Locate every Plasmodium parasite.
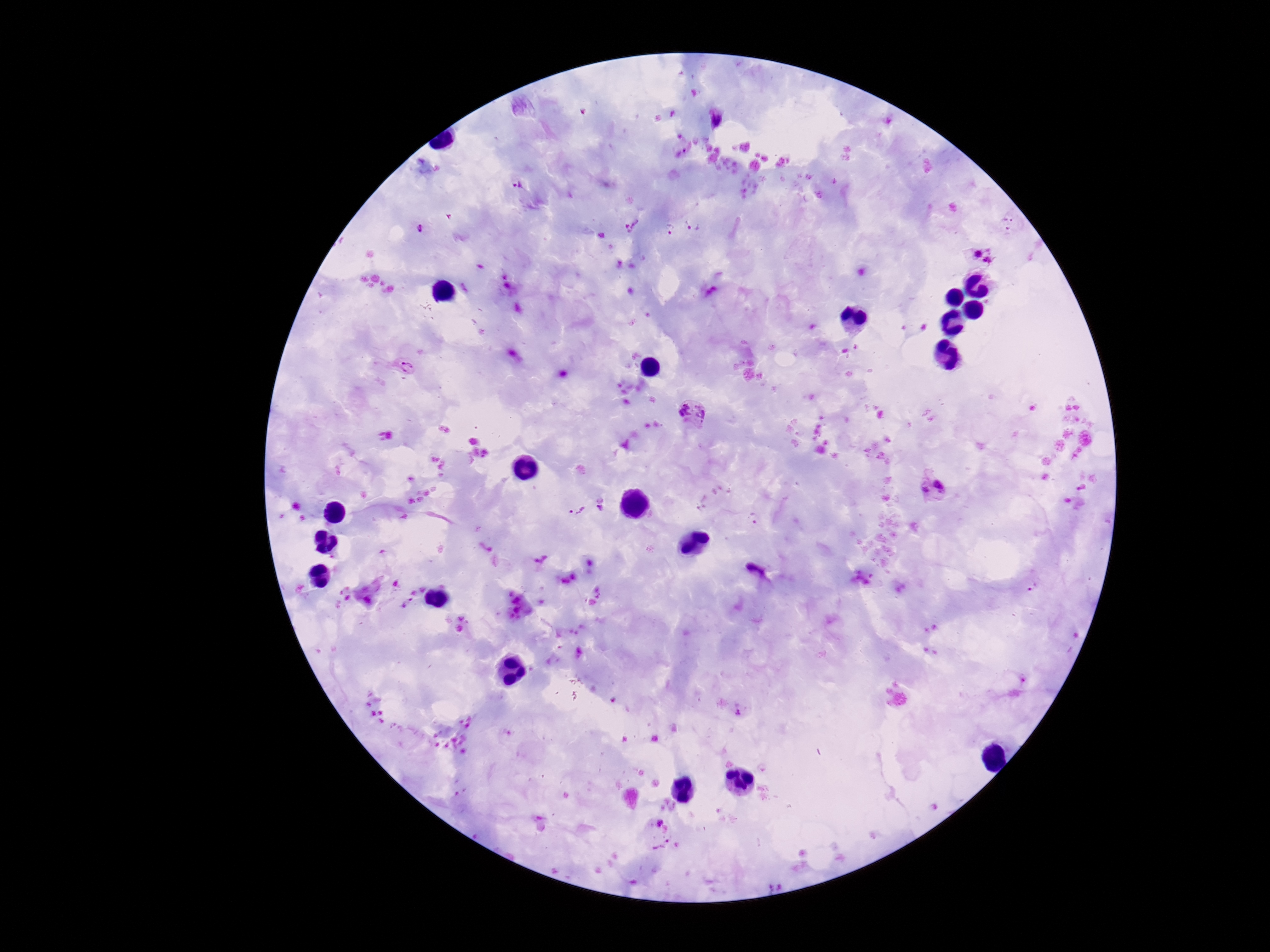

Approximate centers as [x, y] in pixels.
Plasmodium parasites: [718, 118], [517, 185], [1010, 221], [629, 224], [694, 224], [668, 227], [421, 228], [980, 256], [407, 368], [695, 415], [935, 489], [603, 505], [573, 509], [1031, 584], [406, 603], [738, 707], [658, 834].

capture = smartphone camera through the microscope eyepiece
stain = Giemsa
image size = 1270×952 pixels
magnification = 100x
preparation = thick blood film
patient malaria status = positive
field of view = single